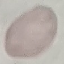
Malaria status: uninfected. Automatically extracted cell patch, resized to 64 × 64 pixels. Thin blood smear. Giemsa stain. Acquired by smartphone through the microscope eyepiece.